Locate every blood parasite and identify its species.
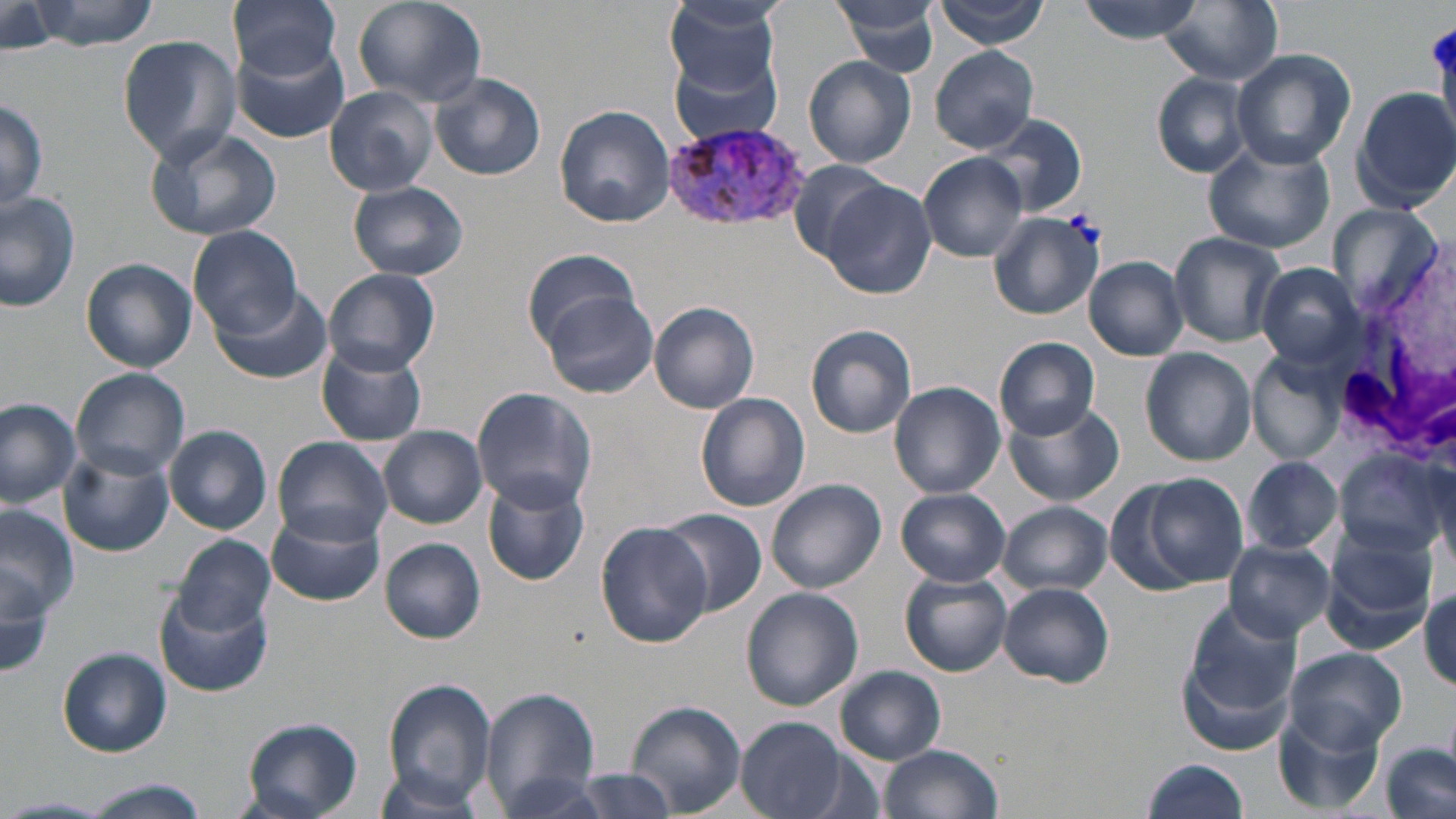
Approximate bounding boxes as (x1,y1)-(x2,y2) corner pairs in pixels.
Plasmodium vivax-infected red blood cells: (658,118)-(816,232).
No Plasmodium falciparum, Plasmodium ovale, Plasmodium malariae, Babesia divergens, or Trypanosoma brucei observed.

slide-level diagnosis = Plasmodium vivax
field of view = single
uninfected red blood cell locations = approximate bounding boxes as (x1,y1)-(x2,y2) corner pairs in pixels: (229,0)-(343,79), (352,0)-(487,108), (664,0)-(783,94), (831,0)-(943,77), (936,0)-(1051,50), (1077,0)-(1206,43), (26,1)-(160,51), (1160,1)-(1285,85), (1,4)-(65,55), (117,35)-(242,162), (233,42)-(350,143), (931,46)-(1040,152), (1232,47)-(1356,170), (671,50)-(786,145), (804,55)-(916,168), (1150,71)-(1256,178), (429,72)-(545,181), (324,85)-(439,197), (1351,85)-(1456,212), (0,94)-(46,216), (554,106)-(674,227), (977,113)-(1087,217), (141,124)-(283,241), (1203,140)-(1337,255), (919,154)-(1028,262), (787,159)-(893,263), (346,180)-(468,281), (823,181)-(936,297), (0,191)-(81,313), (1326,202)-(1446,318), (987,210)-(1102,322), (190,226)-(302,340), (1167,231)-(1286,347), (522,249)-(641,345), (1084,257)-(1189,359), (82,258)-(196,371), (1098,259)-(1209,438), (1255,262)-(1367,369), (324,268)-(440,375), (208,287)-(332,385), (542,290)-(657,398), (649,301)-(760,414), (807,324)-(914,438), (995,337)-(1101,438), (315,340)-(430,448), (1139,347)-(1256,466), (1248,352)-(1347,464), (73,368)-(189,478), (889,382)-(1006,499), (472,386)-(596,514), (696,393)-(809,512), (0,397)-(81,507), (1003,401)-(1124,508), (164,425)-(272,535), (378,426)-(487,528), (272,437)-(394,544), (59,441)-(175,557), (1335,450)-(1449,561), (1242,456)-(1341,554), (1114,471)-(1249,594), (481,475)-(590,588), (766,479)-(886,594), (895,488)-(1011,586), (761,495)-(878,688), (998,501)-(1112,596), (1,503)-(80,635), (267,507)-(382,607), (656,510)-(765,618), (595,521)-(714,649), (170,535)-(275,634), (1319,537)-(1437,655), (1,538)-(59,689), (1222,538)-(1337,642), (380,539)-(486,644), (900,571)-(1013,676), (996,582)-(1115,687), (1418,587)-(1455,690), (155,588)-(271,698), (741,588)-(864,711), (1180,602)-(1305,730), (1282,646)-(1410,752), (56,647)-(172,757), (836,666)-(946,763), (383,676)-(496,811), (478,687)-(603,814), (624,700)-(746,815), (1275,715)-(1383,814), (736,716)-(853,819), (240,718)-(364,819), (877,743)-(1005,819), (1380,745)-(1453,819), (1140,759)-(1251,819), (551,768)-(688,817), (370,769)-(489,817), (495,773)-(619,818), (78,779)-(210,818), (0,795)-(117,818)
modality = light microscopy
image size = 1456×819 pixels
white blood cell locations = approximate bounding boxes as (x1,y1)-(x2,y2) corner pairs in pixels: (1333,271)-(1454,459)
magnification = 1000x
stain = May-Grünwald-Giemsa
preparation = thin blood film